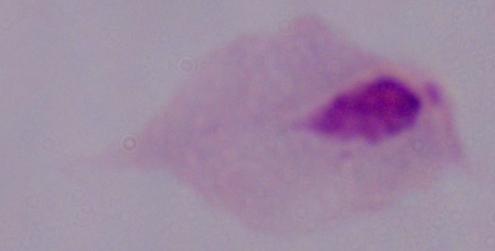
Summary:
  - Magnification: 1000x
  - Identification: trichomonad
  - Modality: photomicrograph